Comment on the morphology of the erythrocytes.
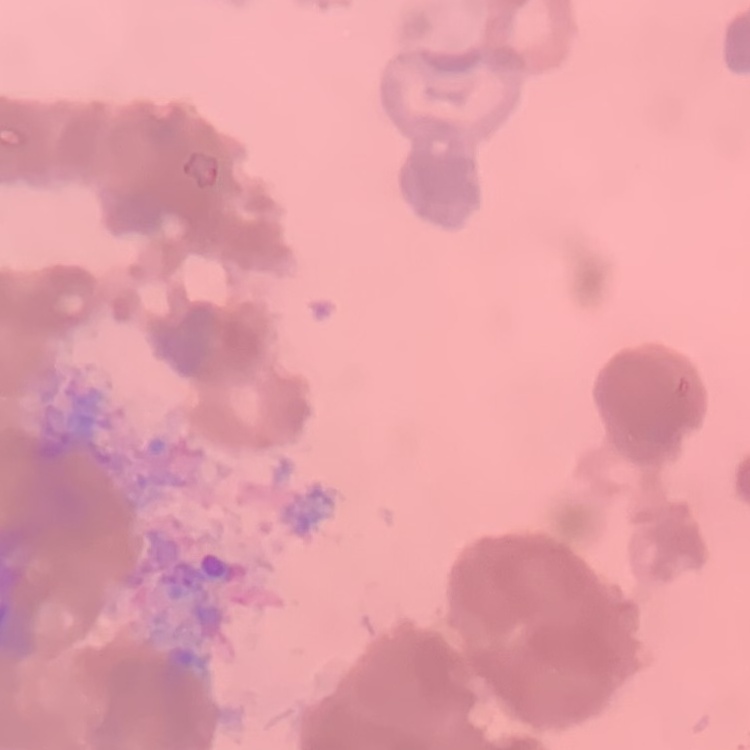

Rouleaux formation.

Summary:
  - Image type: square crop of a larger photomicrograph
  - Preparation: thin blood film
  - Stain: Field's or Giemsa